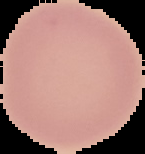

image size = 145×154 pixels
preparation = thin blood smear
result = negative for Plasmodium parasites
image type = cell region segmented out of the field of view; surrounding area masked to black